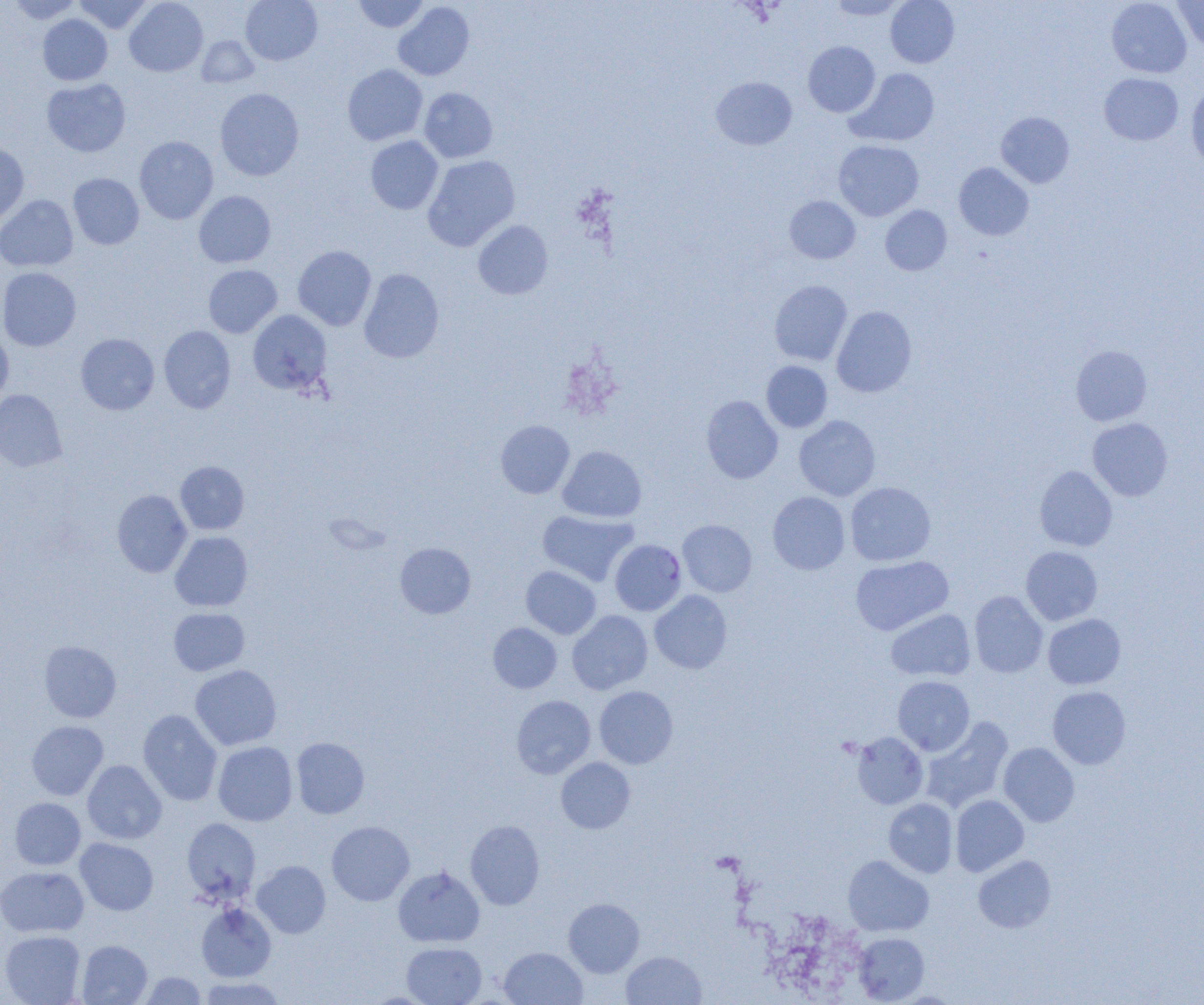

slide-level diagnosis = Plasmodium falciparum
uninfected red blood cell locations = approximate bounding boxes as named x1/y1/x2/y2 corners in pixels: (x1=6, y1=0, x2=84, y2=24), (x1=74, y1=0, x2=151, y2=33), (x1=124, y1=0, x2=208, y2=77), (x1=240, y1=0, x2=322, y2=65), (x1=352, y1=0, x2=429, y2=33), (x1=828, y1=0, x2=907, y2=19), (x1=885, y1=0, x2=959, y2=68), (x1=1106, y1=0, x2=1191, y2=78), (x1=1172, y1=0, x2=1204, y2=51), (x1=393, y1=2, x2=475, y2=80), (x1=37, y1=14, x2=112, y2=85), (x1=196, y1=35, x2=259, y2=88), (x1=803, y1=41, x2=880, y2=117), (x1=342, y1=64, x2=427, y2=146), (x1=847, y1=68, x2=939, y2=147), (x1=1099, y1=73, x2=1183, y2=145), (x1=711, y1=77, x2=797, y2=150), (x1=41, y1=78, x2=131, y2=157), (x1=1185, y1=83, x2=1204, y2=170), (x1=419, y1=87, x2=498, y2=163), (x1=215, y1=88, x2=304, y2=181), (x1=996, y1=112, x2=1074, y2=188), (x1=134, y1=136, x2=218, y2=224), (x1=365, y1=136, x2=443, y2=214), (x1=0, y1=140, x2=29, y2=225), (x1=833, y1=140, x2=923, y2=221), (x1=423, y1=155, x2=520, y2=251), (x1=954, y1=162, x2=1033, y2=241), (x1=68, y1=173, x2=144, y2=250), (x1=194, y1=191, x2=276, y2=268), (x1=0, y1=195, x2=78, y2=272), (x1=785, y1=196, x2=860, y2=264), (x1=880, y1=205, x2=952, y2=275), (x1=473, y1=220, x2=553, y2=300), (x1=293, y1=245, x2=377, y2=330), (x1=204, y1=265, x2=282, y2=337), (x1=0, y1=267, x2=81, y2=351), (x1=359, y1=269, x2=444, y2=363), (x1=770, y1=280, x2=852, y2=365), (x1=832, y1=306, x2=917, y2=398), (x1=248, y1=310, x2=332, y2=395), (x1=159, y1=326, x2=236, y2=413), (x1=0, y1=328, x2=14, y2=407), (x1=76, y1=333, x2=159, y2=415), (x1=1071, y1=345, x2=1152, y2=426), (x1=761, y1=361, x2=832, y2=432), (x1=0, y1=389, x2=67, y2=472), (x1=701, y1=395, x2=783, y2=483), (x1=794, y1=415, x2=880, y2=501), (x1=1087, y1=418, x2=1173, y2=501), (x1=496, y1=420, x2=575, y2=498), (x1=558, y1=446, x2=647, y2=523), (x1=175, y1=461, x2=249, y2=535), (x1=1034, y1=465, x2=1117, y2=551), (x1=845, y1=481, x2=936, y2=566), (x1=112, y1=490, x2=192, y2=577), (x1=767, y1=492, x2=850, y2=574), (x1=537, y1=510, x2=638, y2=586), (x1=678, y1=520, x2=757, y2=596), (x1=169, y1=531, x2=253, y2=611), (x1=395, y1=542, x2=476, y2=619), (x1=1021, y1=546, x2=1102, y2=625), (x1=850, y1=555, x2=953, y2=635), (x1=521, y1=566, x2=601, y2=639), (x1=649, y1=590, x2=732, y2=673), (x1=969, y1=590, x2=1048, y2=678), (x1=168, y1=607, x2=250, y2=676), (x1=886, y1=609, x2=975, y2=682), (x1=567, y1=610, x2=652, y2=694), (x1=1043, y1=613, x2=1126, y2=689), (x1=488, y1=623, x2=562, y2=693), (x1=39, y1=640, x2=121, y2=722), (x1=190, y1=664, x2=282, y2=750), (x1=893, y1=676, x2=974, y2=755), (x1=594, y1=686, x2=678, y2=769), (x1=1048, y1=686, x2=1131, y2=769), (x1=511, y1=695, x2=595, y2=778), (x1=138, y1=709, x2=222, y2=806), (x1=920, y1=716, x2=1014, y2=812), (x1=27, y1=721, x2=108, y2=800), (x1=851, y1=732, x2=928, y2=809), (x1=291, y1=737, x2=369, y2=819), (x1=213, y1=741, x2=298, y2=826), (x1=998, y1=742, x2=1079, y2=827), (x1=556, y1=757, x2=635, y2=834), (x1=82, y1=760, x2=167, y2=844), (x1=950, y1=795, x2=1029, y2=876), (x1=10, y1=797, x2=86, y2=870), (x1=884, y1=798, x2=958, y2=878), (x1=182, y1=817, x2=261, y2=904), (x1=465, y1=820, x2=544, y2=910), (x1=326, y1=821, x2=414, y2=906), (x1=75, y1=837, x2=159, y2=915), (x1=843, y1=855, x2=934, y2=936), (x1=973, y1=855, x2=1056, y2=933), (x1=252, y1=861, x2=331, y2=938), (x1=0, y1=866, x2=88, y2=937), (x1=393, y1=866, x2=485, y2=947), (x1=563, y1=898, x2=644, y2=977), (x1=196, y1=903, x2=276, y2=981), (x1=0, y1=930, x2=85, y2=1004), (x1=853, y1=933, x2=929, y2=1003), (x1=77, y1=939, x2=153, y2=1004), (x1=401, y1=942, x2=487, y2=1004), (x1=499, y1=947, x2=587, y2=1004), (x1=621, y1=951, x2=706, y2=1005), (x1=140, y1=972, x2=207, y2=1004), (x1=197, y1=977, x2=286, y2=1004)
modality = light microscopy
Plasmodium falciparum-infected red blood cell locations = approximate bounding boxes as named x1/y1/x2/y2 corners in pixels: (x1=610, y1=539, x2=686, y2=616)
image size = 1204×1005 pixels
field of view = one of a larger specimen
preparation = thin blood film
magnification = 1000x